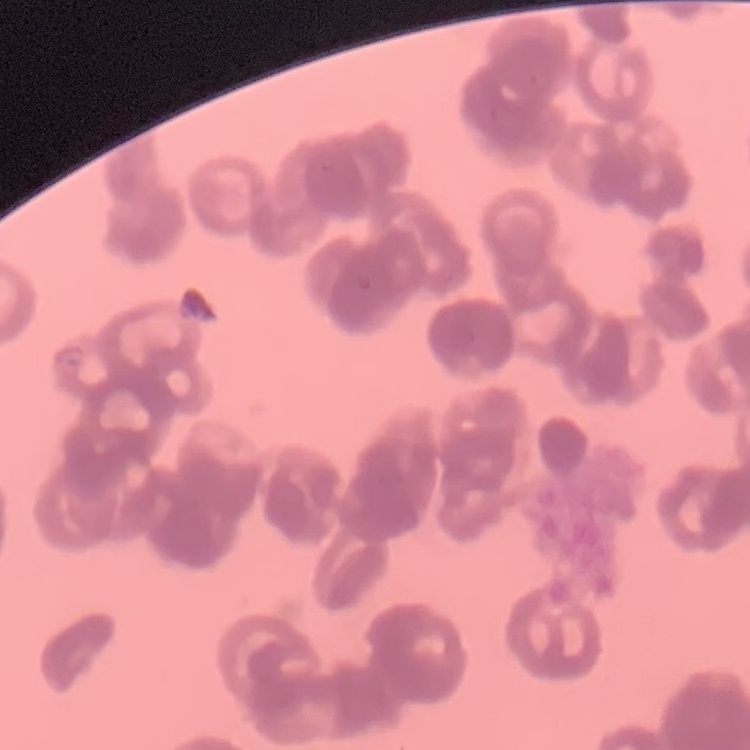
The erythrocytes show rouleaux formation. Stained with either Field's or Giemsa. Square crop of a larger photomicrograph. Thin blood film.